Give the extent of all Plasmodium ovale-infected red blood cells.
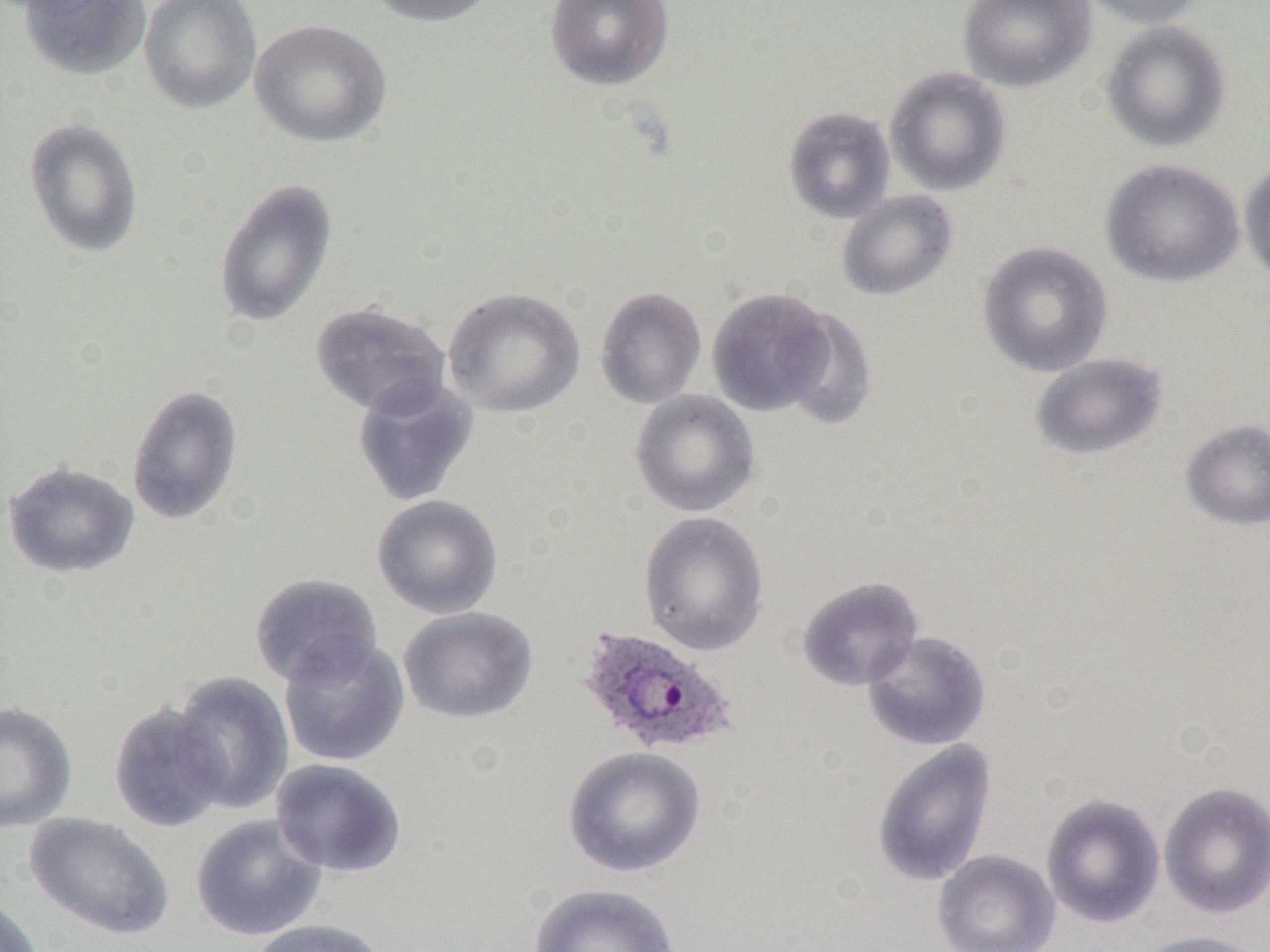

Approximate bounding boxes as (x1,y1)-(x2,y2) corner pairs in pixels.
Plasmodium ovale-infected red blood cells: (576,626)-(739,758).

Summary:
  - Uninfected red blood cell locations: (17,0)-(152,81), (138,0)-(262,114), (363,0)-(500,26), (544,0)-(674,91), (957,0)-(1095,92), (1077,0)-(1209,29), (249,18)-(392,148), (1100,20)-(1232,152), (885,66)-(1012,196), (782,105)-(895,224), (23,116)-(144,258), (1100,158)-(1244,288), (1239,158)-(1270,286), (213,179)-(338,328), (836,190)-(958,301), (977,241)-(1114,377), (444,286)-(585,418), (595,286)-(707,409), (707,287)-(837,418), (309,301)-(451,417), (1030,353)-(1168,460), (351,375)-(480,508), (126,384)-(244,526), (630,389)-(760,517), (1180,418)-(1270,531), (2,459)-(139,579), (372,494)-(504,619), (638,511)-(769,656), (248,572)-(384,688), (796,576)-(925,691), (398,606)-(538,725), (862,630)-(991,751), (278,634)-(410,767), (168,670)-(294,816), (0,701)-(78,833), (107,702)-(228,833), (872,740)-(998,887), (563,745)-(706,878), (270,758)-(407,878), (1159,781)-(1270,920), (1041,793)-(1165,929), (24,812)-(174,941), (190,814)-(328,941), (933,849)-(1060,952), (527,883)-(682,952), (0,896)-(45,952), (248,918)-(391,952), (1131,930)-(1269,952)
  - Slide-level diagnosis: Plasmodium ovale
  - Preparation: thin blood smear
  - Modality: optical microscopy
  - Magnification: 1000x
  - Image size: 1270×952 pixels
  - Field of view: one of a larger specimen